Locate and identify every blood parasite.
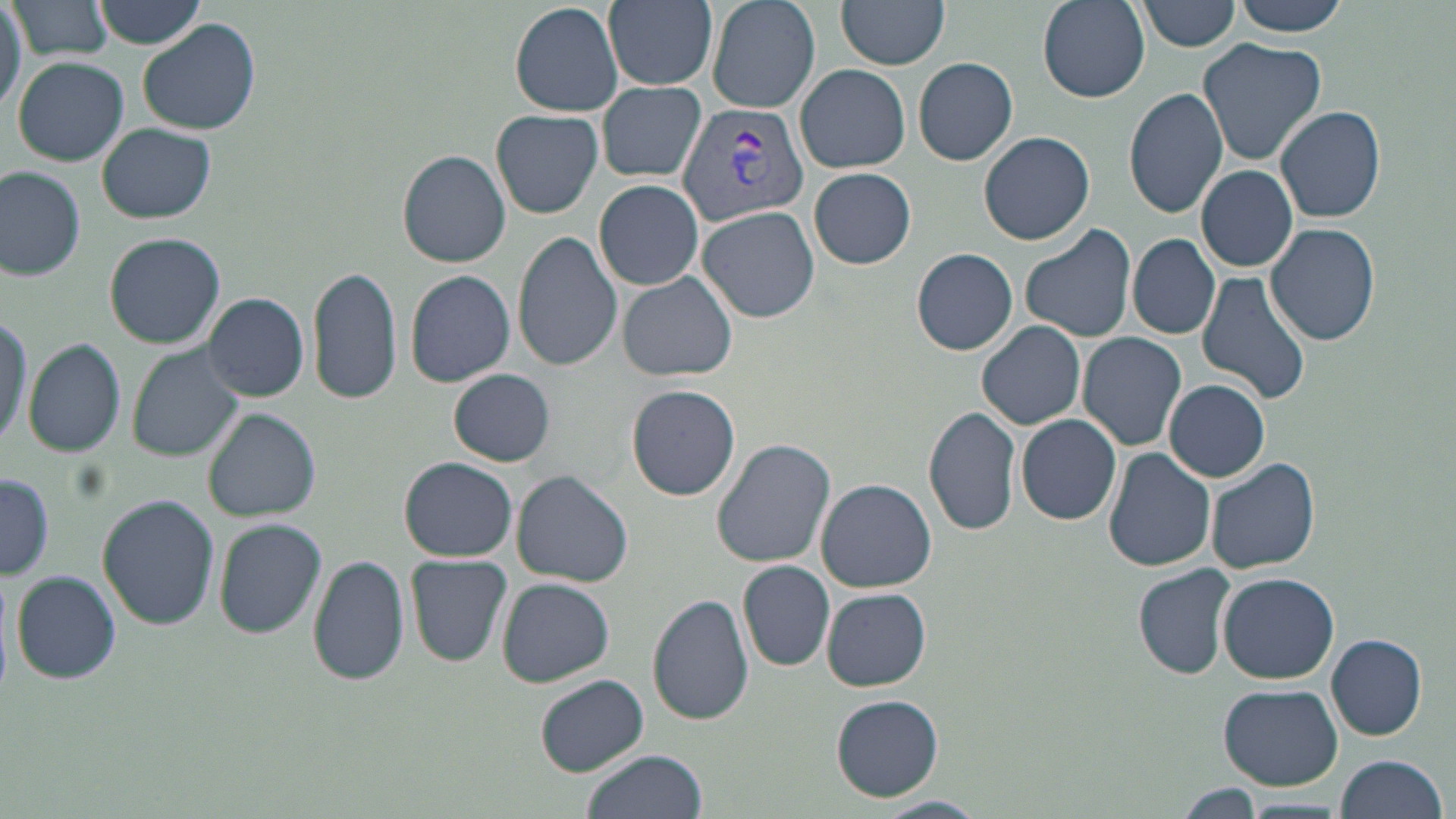

Approximate bounding boxes as [x1, y1, x2, y2] in pixels.
Plasmodium vivax-infected red blood cells: [675, 103, 808, 225].
No Plasmodium falciparum, Plasmodium ovale, Plasmodium malariae, Babesia divergens, or Trypanosoma brucei observed.

Uninfected red blood cell locations: [0, 0, 27, 107], [11, 0, 116, 61], [95, 0, 209, 48], [604, 0, 717, 90], [706, 0, 821, 115], [838, 0, 949, 71], [1035, 0, 1150, 104], [1140, 0, 1241, 52], [1231, 0, 1351, 36], [511, 1, 625, 116], [139, 20, 260, 135], [1198, 37, 1326, 165], [913, 57, 1019, 166], [12, 58, 128, 166], [795, 65, 910, 173], [598, 80, 707, 183], [1124, 86, 1230, 219], [1274, 105, 1389, 222], [490, 109, 604, 219], [99, 122, 217, 223], [979, 131, 1095, 246], [398, 149, 511, 267], [991, 158, 1112, 324], [1196, 164, 1299, 271], [808, 167, 916, 270], [0, 169, 86, 279], [594, 180, 704, 290], [697, 205, 819, 322], [1019, 223, 1136, 343], [1264, 224, 1380, 348], [514, 230, 622, 371], [105, 233, 226, 349], [1128, 234, 1219, 339], [912, 249, 1018, 354], [308, 265, 402, 404], [404, 269, 516, 388], [1196, 271, 1312, 405], [618, 273, 736, 381], [203, 293, 310, 400], [0, 314, 31, 445], [977, 320, 1085, 430], [1078, 332, 1187, 450], [23, 338, 128, 457], [127, 343, 244, 462], [448, 368, 556, 467], [1165, 379, 1270, 482], [626, 383, 740, 501], [923, 405, 1022, 537], [205, 408, 321, 522], [1017, 414, 1121, 525], [712, 439, 836, 571], [1103, 447, 1214, 572], [1207, 456, 1320, 574], [400, 458, 517, 562], [513, 471, 634, 587], [0, 476, 55, 580], [817, 478, 937, 592], [98, 495, 219, 629], [214, 519, 326, 640], [308, 553, 410, 687], [405, 554, 513, 667], [738, 560, 835, 671], [1136, 562, 1235, 677], [12, 571, 119, 685], [1218, 572, 1341, 682], [495, 577, 615, 687], [822, 587, 930, 691], [648, 592, 756, 725], [1326, 634, 1428, 740], [535, 674, 648, 775], [1217, 684, 1346, 788], [832, 695, 943, 801], [581, 749, 708, 819], [1334, 754, 1446, 819], [1179, 784, 1267, 815], [873, 798, 985, 819], [1237, 799, 1351, 818]. Slide-level diagnosis: Plasmodium vivax. One field of a larger specimen. Thin blood film. Image is 1456×819 pixels. 1000x magnification. May-Grünwald-Giemsa stain. Light microscopy.